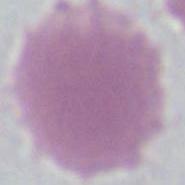
magnification = 1000x
identification = erythrocyte
modality = photomicrograph